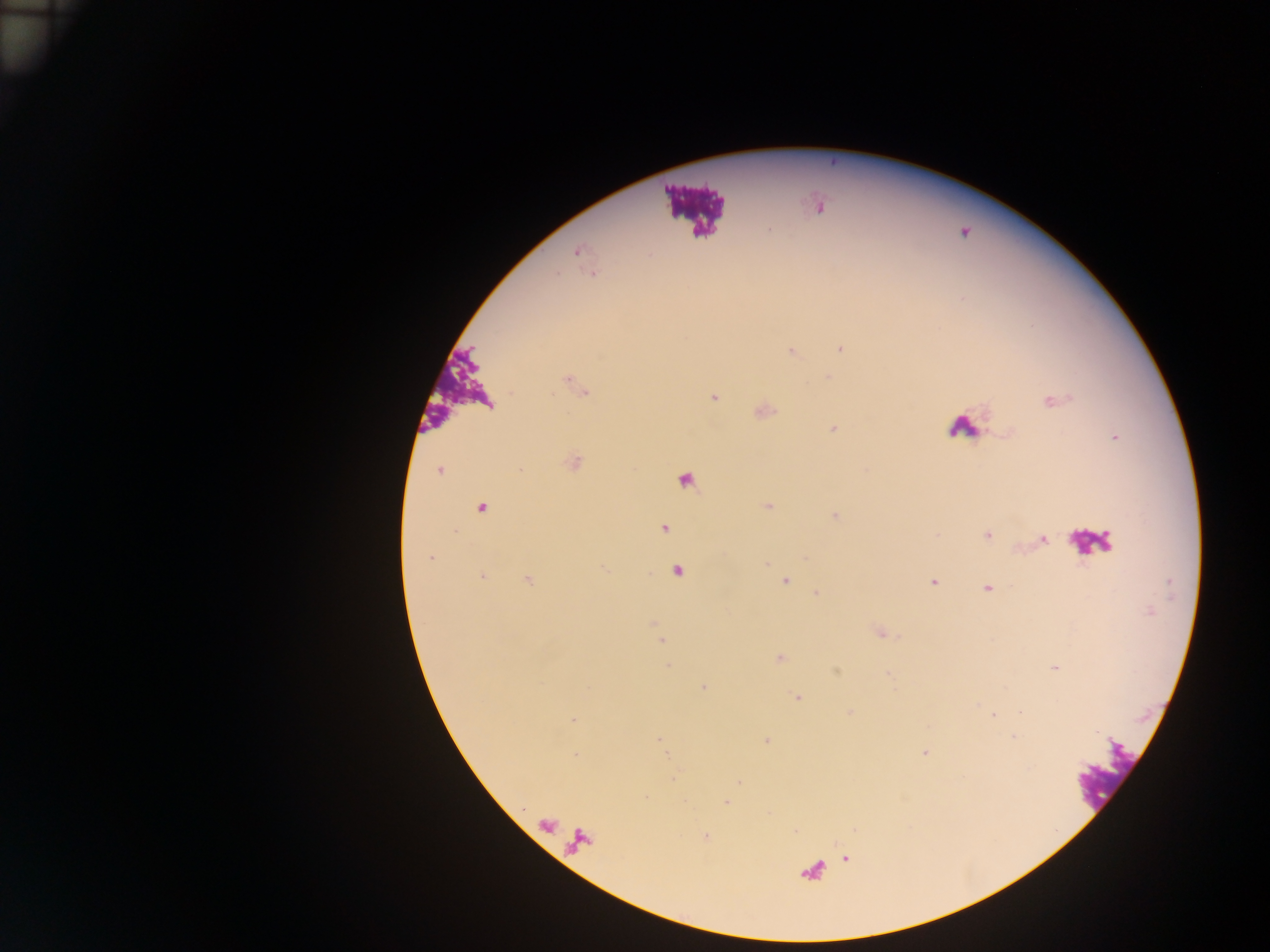
preparation = thick blood film
field of view = single
country = Ghana
leukocyte locations = approximate centers as [x, y] in pixels: [692, 208], [450, 384], [963, 428], [1092, 542], [1109, 770]
image size = 1270×952 pixels
Plasmodium parasite locations = approximate centers as [x, y] in pixels: [578, 251], [840, 349], [790, 351], [566, 380], [714, 398], [1053, 401], [834, 428], [439, 471], [768, 505], [481, 507], [836, 516], [664, 528], [988, 536], [1043, 540], [430, 558], [678, 571], [483, 577], [528, 579], [786, 580], [933, 582], [987, 588], [816, 593], [881, 634], [662, 641], [780, 658], [668, 666], [1055, 667], [704, 687], [797, 698], [994, 714], [573, 720], [660, 738], [1014, 738], [766, 740], [924, 752], [575, 755], [673, 778], [726, 802]
capture = mobile-phone photograph through a microscope